Locate and identify every blood parasite.
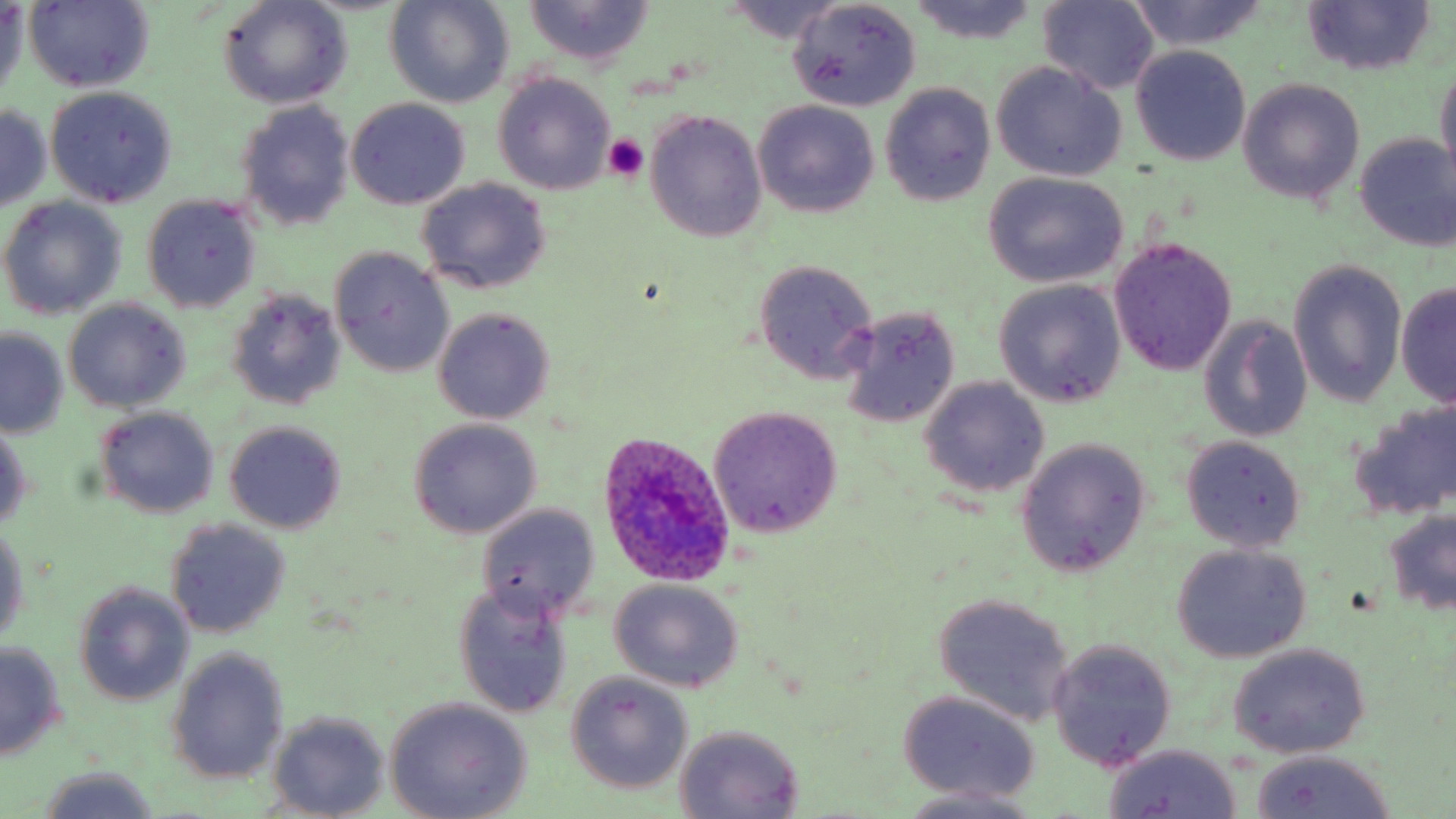
Approximate bounding boxes as (x1,y1)-(x2,y2) corner pairs in pixels.
Plasmodium ovale-infected red blood cells: (590,432)-(739,591).
No Plasmodium falciparum, Plasmodium malariae, Plasmodium vivax, Babesia divergens, or Trypanosoma brucei observed.

slide_level_diagnosis: Plasmodium ovale
field_of_view: single
platelet_locations: 'approximate bounding boxes as (x1,y1)-(x2,y2) corner pairs in pixels: (602,134)-(647,181)'
image_size: 1456×819 pixels
stain: May-Grünwald-Giemsa
uninfected_red_blood_cell_locations: 'approximate bounding boxes as (x1,y1)-(x2,y2) corner pairs in pixels: (385,0)-(512,108), (789,0)-(922,111), (910,0)-(1038,44), (218,1)-(352,109), (520,1)-(656,66), (721,1)-(851,43), (1122,1)-(1273,49), (24,2)-(155,90), (1039,2)-(1159,95), (1301,2)-(1437,76), (1,3)-(27,100), (1130,46)-(1251,166), (991,61)-(1129,181), (1434,62)-(1456,186), (493,72)-(617,195), (1237,79)-(1365,205), (879,82)-(995,208), (45,86)-(177,207), (347,98)-(470,208), (236,101)-(355,232), (752,101)-(879,218), (0,106)-(52,211), (644,111)-(768,242), (1353,132)-(1456,250), (983,173)-(1128,287), (416,177)-(551,294), (143,196)-(262,313), (0,198)-(127,320), (1109,237)-(1236,376), (329,248)-(455,377), (752,259)-(880,384), (1288,259)-(1407,408), (995,280)-(1127,407), (1396,281)-(1455,407), (226,289)-(345,409), (65,299)-(189,413), (838,306)-(963,429), (432,307)-(555,424), (1198,316)-(1311,441), (1,328)-(68,437), (920,376)-(1048,499), (1353,402)-(1456,520), (95,405)-(220,518), (707,406)-(842,538), (408,417)-(542,539), (222,420)-(348,535), (0,421)-(32,532), (1180,435)-(1306,552), (1015,440)-(1151,576), (474,505)-(599,621), (1382,507)-(1456,617), (164,518)-(291,640), (0,523)-(27,646), (1172,544)-(1312,662), (609,579)-(743,692), (452,582)-(575,719), (73,584)-(193,706), (932,593)-(1075,726), (1047,639)-(1177,771), (0,640)-(68,760), (1227,644)-(1370,759), (164,647)-(290,786), (564,672)-(693,795), (896,691)-(1044,803), (384,699)-(533,817), (268,712)-(390,819), (672,724)-(805,817), (1102,743)-(1243,818), (1249,748)-(1398,819), (35,768)-(164,819), (897,787)-(1048,818)'
modality: light microscopy
magnification: 1000x
preparation: thin blood film